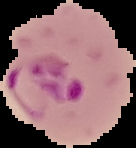

Summary:
  - Preparation: thin blood smear
  - Image type: cell region segmented out of the field of view; surrounding area masked to black
  - Result: Plasmodium parasites detected
  - Image size: 136×148 pixels